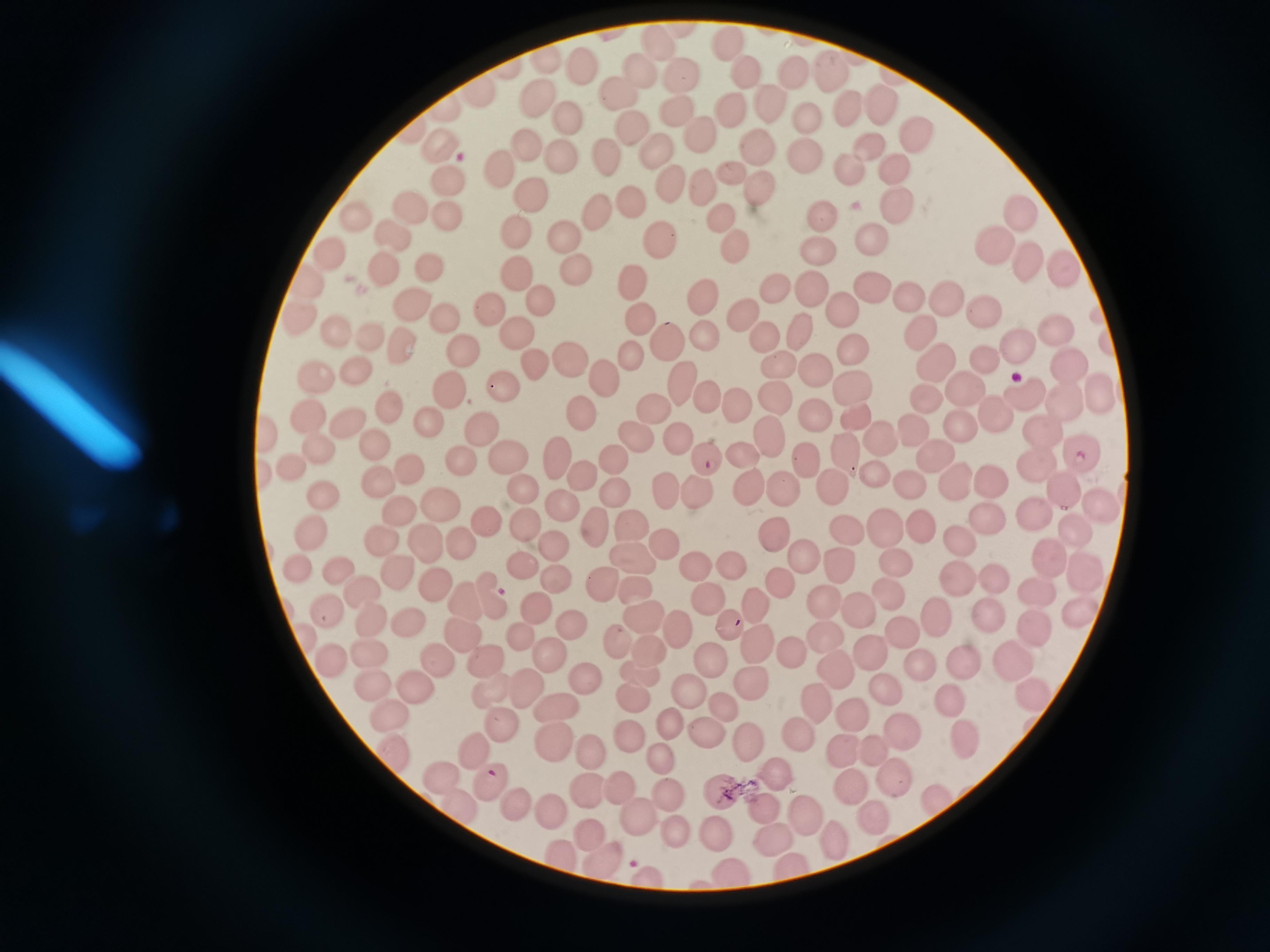

cell locations = approximate centers as (x, y) in pixels: (730, 43), (661, 48), (550, 61), (742, 67), (581, 70), (793, 73), (830, 74), (637, 76), (679, 76), (477, 93), (618, 97), (537, 101), (771, 103), (884, 106), (728, 108), (848, 110), (679, 111), (810, 115), (566, 118), (631, 127), (916, 133), (702, 135), (523, 145), (867, 145), (757, 148), (440, 151), (658, 152), (806, 153), (605, 154), (562, 158), (892, 164), (849, 167), (499, 168), (732, 169), (445, 183), (754, 183), (702, 185), (671, 187), (532, 194), (412, 197), (631, 203), (893, 210), (598, 212), (721, 216), (448, 218), (824, 218), (1025, 219), (355, 220), (515, 228), (393, 235), (564, 236), (657, 237), (866, 237), (815, 246), (733, 247), (992, 248), (328, 255), (1024, 258), (1066, 266), (429, 268), (381, 269), (520, 271), (576, 271), (308, 280), (631, 282), (871, 283), (810, 286), (772, 288), (907, 294), (701, 295), (944, 298), (546, 303), (414, 304), (840, 306), (493, 309), (983, 309), (301, 317), (448, 318), (744, 318), (638, 320), (331, 327), (798, 329), (517, 331), (916, 334), (1054, 334), (706, 335), (371, 337), (666, 338), (765, 339), (1014, 343), (852, 345), (402, 348), (461, 354), (630, 356), (987, 357), (568, 360), (532, 361), (934, 364), (1068, 365), (356, 366), (781, 366), (813, 368), (317, 376), (682, 379), (601, 381), (959, 384), (501, 386), (851, 386), (447, 389), (925, 394), (705, 395), (1099, 395), (775, 396), (1026, 399), (1064, 402), (735, 404), (388, 405), (656, 409), (582, 415), (813, 415), (309, 416), (994, 416), (856, 417), (346, 418), (426, 422), (910, 425), (958, 425), (477, 427), (1042, 429), (266, 434), (768, 434), (878, 437), (683, 439), (633, 440), (373, 444), (320, 448), (1081, 449), (842, 451), (804, 454), (505, 457), (742, 457), (935, 458), (553, 459), (462, 460), (706, 460), (618, 462), (1033, 464), (293, 467), (408, 468), (877, 472), (580, 474), (380, 479), (952, 482), (829, 483), (993, 483), (906, 484), (751, 486), (782, 487), (521, 488), (614, 490), (1063, 490), (665, 491), (695, 494), (323, 495), (438, 504), (560, 505), (1100, 507), (397, 509), (1035, 512), (983, 516), (484, 521), (885, 522), (523, 523), (629, 526), (596, 527), (920, 527), (1075, 527), (846, 529), (313, 531), (771, 532), (379, 539), (422, 540), (959, 541), (660, 542), (458, 543), (556, 546), (800, 551), (1046, 551), (630, 558), (838, 561), (894, 561), (520, 563), (726, 564), (299, 566), (690, 566), (1081, 567), (337, 573), (399, 575), (992, 576), (957, 578), (604, 580), (435, 582), (781, 582), (560, 584), (636, 585), (359, 590), (894, 590), (1036, 590), (707, 599), (466, 600), (488, 600), (759, 604), (827, 604), (536, 606), (324, 610), (990, 610), (861, 614), (1081, 614), (640, 615), (937, 615), (373, 622), (411, 622), (571, 623), (1037, 626), (901, 627), (734, 629), (680, 632), (822, 633), (517, 634), (618, 637), (308, 638), (460, 638), (758, 644), (648, 649), (872, 650), (791, 653), (372, 655), (1014, 656), (552, 657), (714, 658), (432, 659), (326, 660), (479, 660), (963, 661), (920, 662), (831, 663), (642, 672), (583, 680), (752, 680), (371, 683), (410, 683), (530, 689), (690, 690), (490, 692), (884, 692), (1033, 694), (942, 696), (633, 701), (815, 703), (552, 706), (385, 710), (727, 710), (854, 712), (495, 722), (674, 725), (796, 731), (704, 733), (899, 733), (963, 738), (633, 740), (747, 741), (844, 747), (871, 747), (552, 748), (589, 748), (390, 749), (478, 751), (665, 759), (776, 769), (439, 771), (890, 780), (624, 781), (491, 782), (586, 787), (855, 788), (718, 789), (934, 794), (668, 796), (453, 802), (515, 805), (764, 805), (549, 808), (802, 811), (639, 814), (871, 816), (717, 832), (773, 833), (591, 834), (673, 834), (835, 836), (564, 855), (602, 862), (793, 866), (730, 871), (649, 878)
capture = smartphone through the microscope eyepiece
image size = 1270×952 pixels
field of view = single
stain = Giemsa
preparation = thin blood film